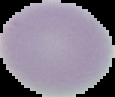
image type = segmented cell region on a black background
malaria status = uninfected
preparation = thin blood film
image size = 115×97 pixels